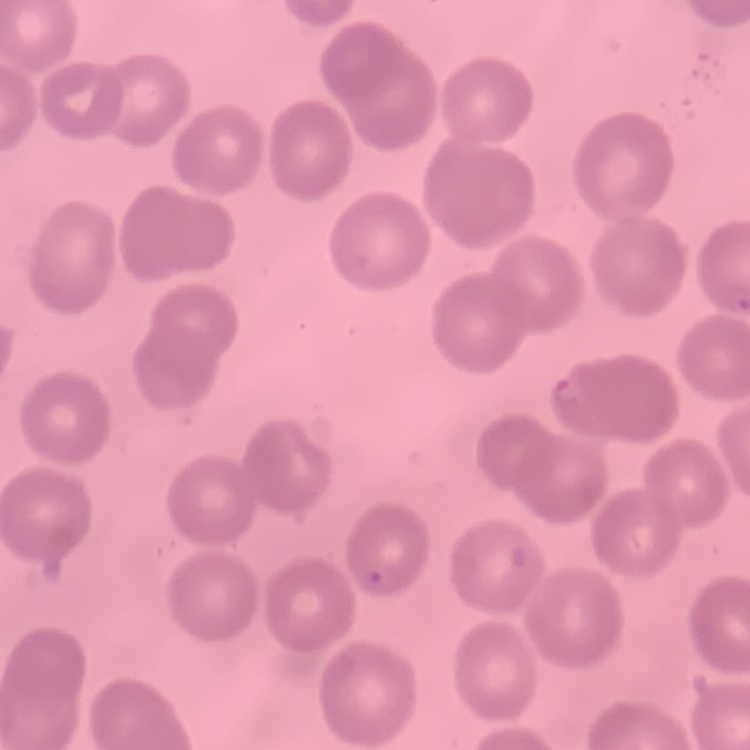
red blood cell morphology = no rouleaux formation
preparation = thin blood film
image type = one tile cut from a larger photomicrograph
stain = Field's or Giemsa